Classify this cell by malaria status.
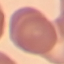
It is uninfected.

Summary:
  - Stain: Giemsa
  - Image type: cell patch, automatically extracted from a larger field of view and resized to 64 × 64 pixels
  - Preparation: thin blood film
  - Capture: smartphone through the microscope eyepiece